Report the malaria status of this cell.
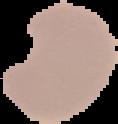
Parasitized.

From a thin blood smear. Segmented cell region on a black background. Image is 118×124 pixels.